Report the malaria status of this cell.
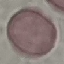
It is uninfected.

Summary:
  - Capture: smartphone camera at the microscope eyepiece
  - Preparation: thin blood smear
  - Image type: cell patch, automatically extracted from a larger field of view and resized to 64 × 64 pixels
  - Stain: Giemsa